Comment on the morphology of the red blood cells.
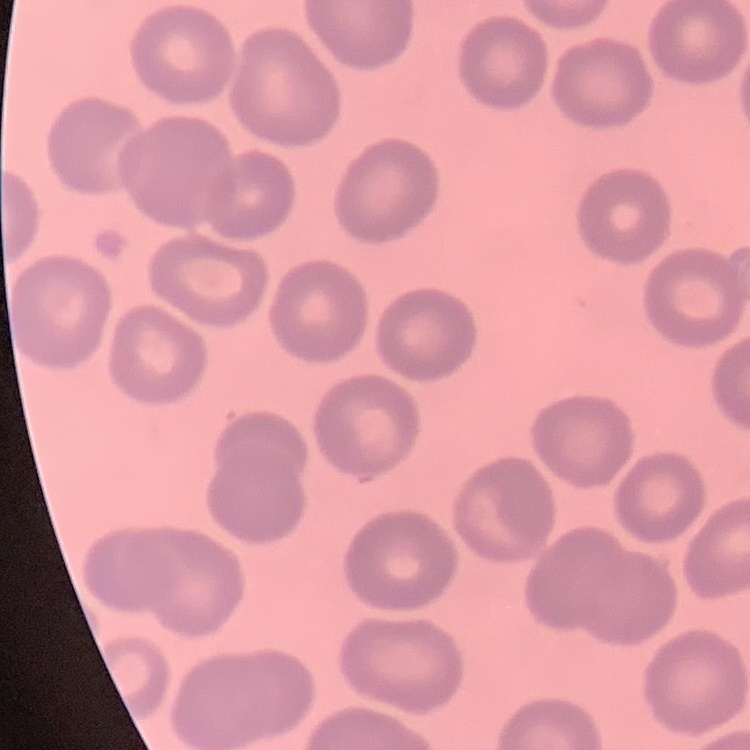
They show no rouleaux formation.

Summary:
  - Stain: Field's or Giemsa
  - Image type: one tile cut from a larger photomicrograph
  - Preparation: thin peripheral smear